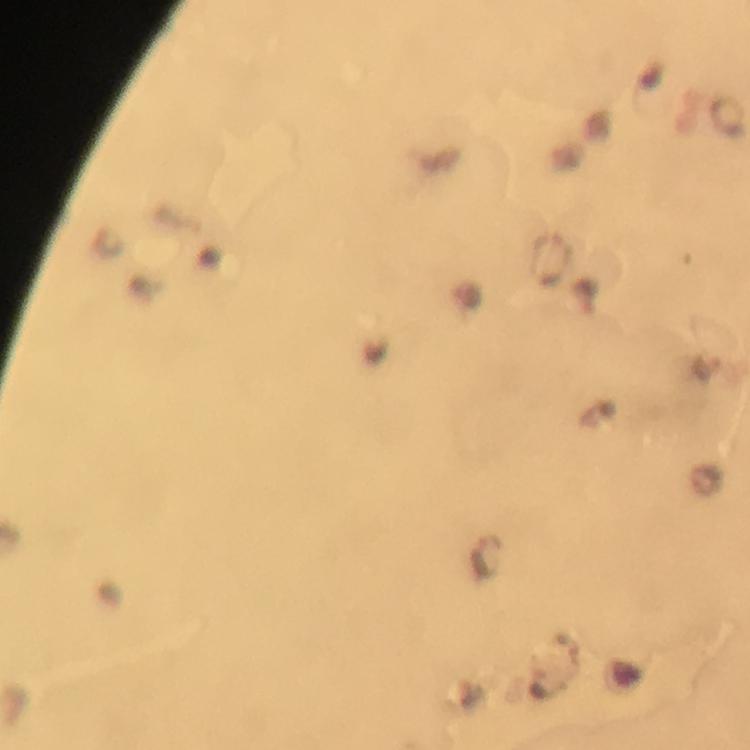
Approximate object centers, in pixels from the top-left corner.
Summary:
  - Malaria parasite locations: (x=550, y=258), (x=589, y=297), (x=707, y=367), (x=487, y=557)
  - Preparation: thick blood film
  - Immersion oil: applied
  - Context: from a diagnostic examination for malaria
  - Cropped from: one field of view
  - Magnification: 100x
  - Stain: Giemsa
  - Image size: 750×750 pixels
  - Capture: smartphone camera through the microscope